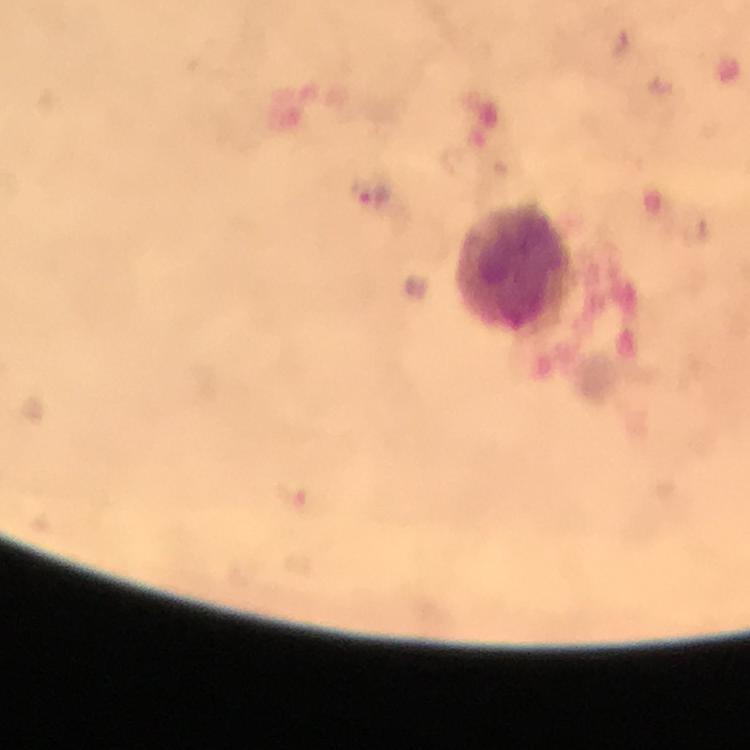
Approximate centers as {x, y} in pixels.
Summary:
  - Plasmodium parasite locations: {369, 194}
  - Leukocyte locations: {515, 267}
  - Immersion oil: applied
  - Capture: smartphone photograph through a microscope
  - Context: from a diagnostic examination for malaria
  - Stain: Giemsa
  - Cropped from: one field of view
  - Image size: 750×750 pixels
  - Magnification: 100x
  - Preparation: thick blood film